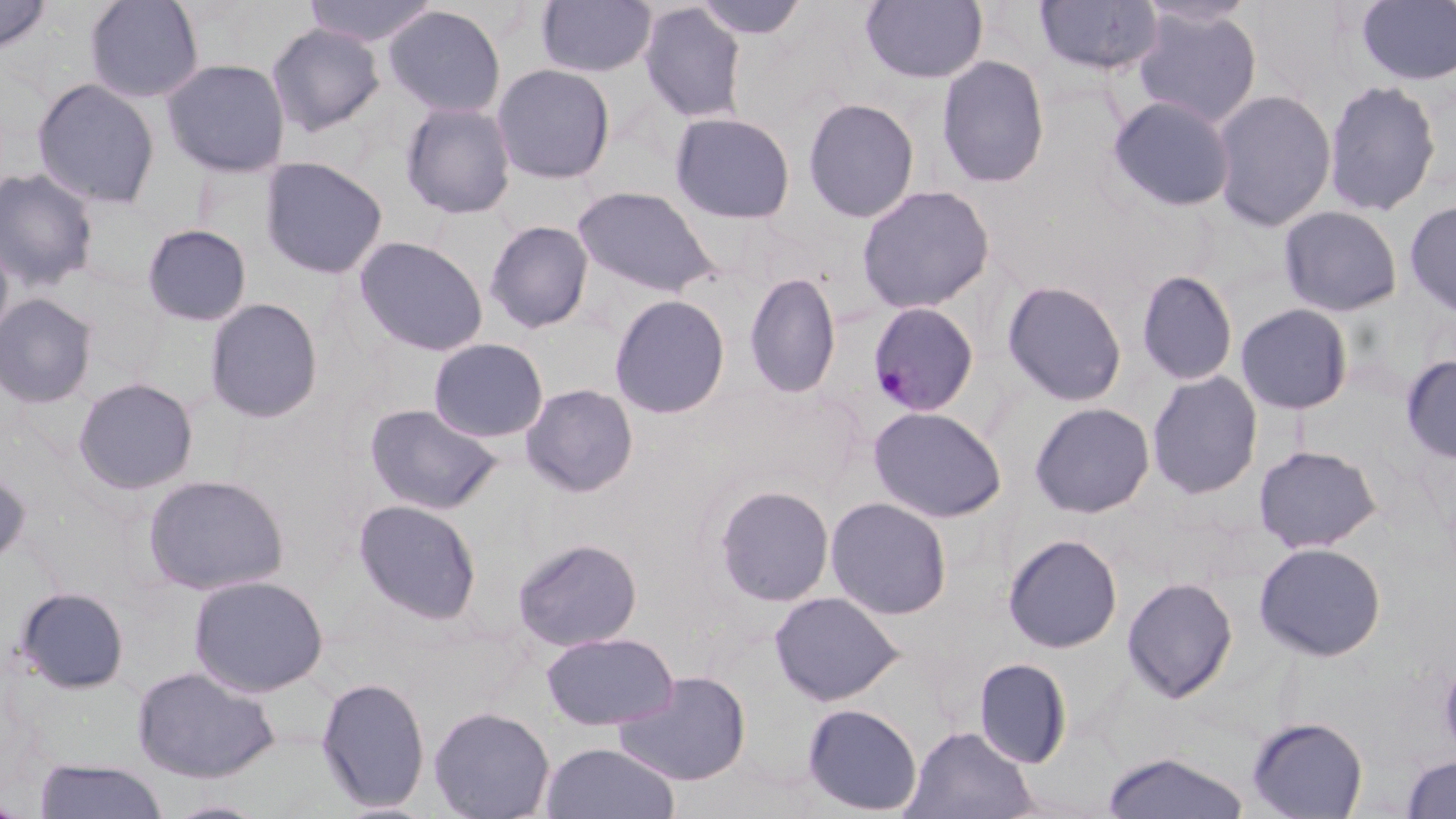

slide_level_diagnosis: Plasmodium malariae
preparation: thin blood smear
modality: light microscopy
field_of_view: single
stain: May-Grünwald-Giemsa
uninfected_red_blood_cell_locations: 'approximate bounding boxes as (x1,y1)-(x2,y2) corner pairs in pixels: (0,0)-(52,56), (83,0)-(205,104), (302,0)-(440,47), (537,0)-(657,77), (693,0)-(809,40), (860,0)-(988,84), (1033,1)-(1163,78), (1356,1)-(1456,86), (638,2)-(747,124), (383,5)-(507,119), (1131,6)-(1263,128), (266,22)-(385,137), (936,55)-(1050,188), (161,57)-(291,178), (491,62)-(616,184), (31,77)-(161,210), (1323,79)-(1442,217), (1211,88)-(1337,231), (1107,95)-(1236,212), (802,97)-(920,223), (399,100)-(518,220), (669,112)-(797,225), (259,156)-(388,280), (0,167)-(100,292), (856,184)-(995,314), (572,185)-(721,297), (1403,199)-(1456,320), (1279,205)-(1404,317), (485,219)-(594,334), (141,224)-(252,327), (0,234)-(15,354), (353,235)-(489,357), (1135,268)-(1239,387), (743,272)-(841,399), (1001,279)-(1128,407), (0,293)-(99,409), (609,294)-(731,419), (204,298)-(324,423), (1234,303)-(1355,415), (428,337)-(549,443), (1400,354)-(1456,464), (1147,371)-(1264,500), (72,377)-(199,495), (521,383)-(639,497), (1029,402)-(1156,518), (364,403)-(503,516), (868,405)-(1008,523), (1253,444)-(1382,553), (0,464)-(32,570), (142,473)-(289,595), (714,484)-(835,606), (825,496)-(953,620), (353,498)-(483,625), (1002,533)-(1123,654), (512,537)-(643,651), (1254,541)-(1387,662), (187,573)-(329,698), (1121,576)-(1238,703), (13,586)-(131,695), (769,591)-(903,706), (541,631)-(679,731), (1439,652)-(1456,764), (972,657)-(1073,769), (130,664)-(281,784), (613,670)-(751,786), (315,676)-(431,813), (801,702)-(923,816), (428,706)-(556,819), (1246,715)-(1368,819), (902,725)-(1037,819), (540,742)-(681,819), (1101,751)-(1251,818), (1401,755)-(1456,817), (34,759)-(169,819), (162,800)-(273,819)'
plasmodium_malariae_infected_red_blood_cell_locations: 'approximate bounding boxes as (x1,y1)-(x2,y2) corner pairs in pixels: (867,301)-(981,417)'
image_size: 1456×819 pixels
magnification: 1000x